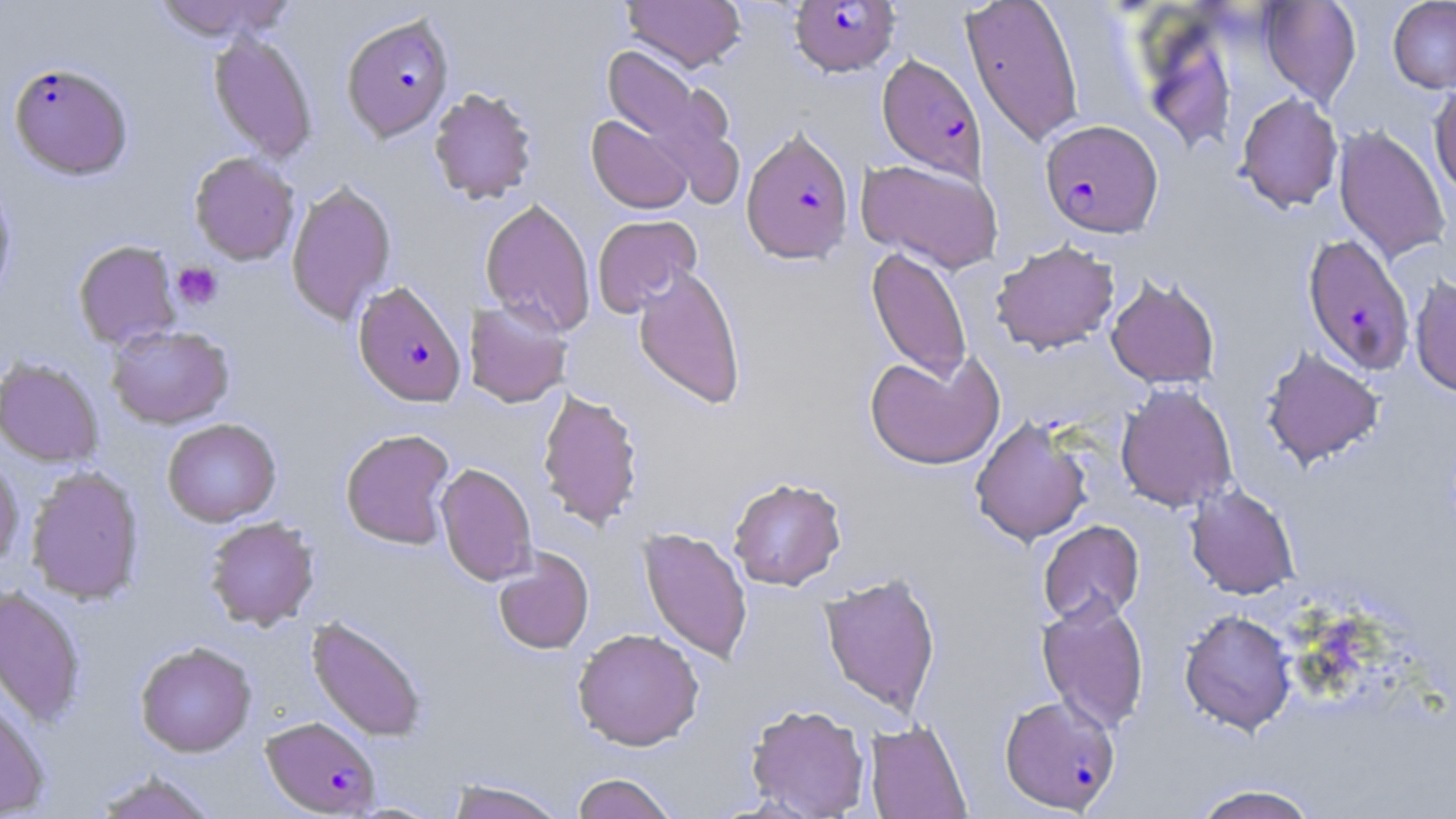
Approximate bounding boxes as named x1/y1/x2/y2 corners in pixels. Uninfected red blood cell locations: (x1=150, y1=0, x2=297, y2=42), (x1=622, y1=0, x2=746, y2=72), (x1=960, y1=0, x2=1085, y2=149), (x1=1260, y1=0, x2=1361, y2=108), (x1=1388, y1=0, x2=1456, y2=93), (x1=1141, y1=25, x2=1237, y2=155), (x1=208, y1=31, x2=317, y2=162), (x1=600, y1=43, x2=728, y2=175), (x1=1429, y1=83, x2=1456, y2=198), (x1=429, y1=87, x2=538, y2=204), (x1=1236, y1=92, x2=1343, y2=212), (x1=586, y1=115, x2=692, y2=213), (x1=1333, y1=124, x2=1452, y2=264), (x1=189, y1=152, x2=300, y2=265), (x1=856, y1=158, x2=1003, y2=273), (x1=0, y1=173, x2=17, y2=310), (x1=286, y1=180, x2=397, y2=325), (x1=479, y1=198, x2=596, y2=336), (x1=592, y1=215, x2=702, y2=317), (x1=73, y1=239, x2=182, y2=349), (x1=991, y1=240, x2=1120, y2=354), (x1=866, y1=247, x2=972, y2=384), (x1=632, y1=266, x2=747, y2=410), (x1=1105, y1=275, x2=1221, y2=389), (x1=1410, y1=275, x2=1456, y2=397), (x1=464, y1=300, x2=571, y2=408), (x1=106, y1=324, x2=234, y2=429), (x1=1260, y1=347, x2=1384, y2=469), (x1=864, y1=351, x2=1004, y2=470), (x1=0, y1=357, x2=104, y2=467), (x1=1115, y1=383, x2=1238, y2=512), (x1=537, y1=388, x2=643, y2=530), (x1=970, y1=416, x2=1093, y2=546), (x1=162, y1=418, x2=281, y2=526), (x1=340, y1=428, x2=456, y2=549), (x1=0, y1=455, x2=23, y2=570), (x1=435, y1=462, x2=537, y2=585), (x1=26, y1=466, x2=144, y2=604), (x1=728, y1=476, x2=847, y2=590), (x1=1185, y1=484, x2=1300, y2=599), (x1=204, y1=516, x2=319, y2=630), (x1=1038, y1=520, x2=1145, y2=626), (x1=638, y1=527, x2=753, y2=664), (x1=493, y1=547, x2=594, y2=654), (x1=819, y1=572, x2=941, y2=716), (x1=0, y1=585, x2=87, y2=728), (x1=1037, y1=594, x2=1150, y2=734), (x1=1179, y1=609, x2=1297, y2=736), (x1=306, y1=616, x2=428, y2=742), (x1=572, y1=628, x2=704, y2=750), (x1=135, y1=641, x2=256, y2=757), (x1=0, y1=687, x2=51, y2=818), (x1=745, y1=703, x2=870, y2=818), (x1=864, y1=721, x2=972, y2=819), (x1=92, y1=770, x2=220, y2=819), (x1=571, y1=772, x2=679, y2=819), (x1=445, y1=778, x2=568, y2=819), (x1=1189, y1=783, x2=1322, y2=819). Plasmodium falciparum-infected red blood cell locations: (x1=789, y1=1, x2=901, y2=76), (x1=341, y1=13, x2=454, y2=141), (x1=876, y1=53, x2=987, y2=183), (x1=9, y1=61, x2=133, y2=179), (x1=1040, y1=119, x2=1163, y2=238), (x1=741, y1=127, x2=854, y2=264), (x1=1302, y1=234, x2=1415, y2=376), (x1=353, y1=280, x2=466, y2=407), (x1=999, y1=694, x2=1121, y2=814), (x1=260, y1=716, x2=381, y2=816). Platelet locations: (x1=172, y1=261, x2=223, y2=310). Slide-level diagnosis: Plasmodium falciparum. 1000x magnification. Light microscopy. May-Grünwald-Giemsa-stained preparation. Image is 1456×819 pixels. Thin blood smear. Single field of view.